Assess this cell for malaria.
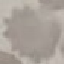
It is uninfected.

{
  "stain": "Giemsa",
  "capture": "smartphone camera at the microscope eyepiece",
  "image_type": "cell patch, automatically extracted from a larger field of view and resized to 64 × 64 pixels",
  "preparation": "thin blood film"
}